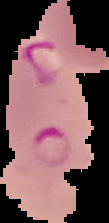 Cell region segmented out of the field of view; the surrounding area is masked to black. Image is 109×223 pixels. Malaria status: parasitized. From a thin blood film.